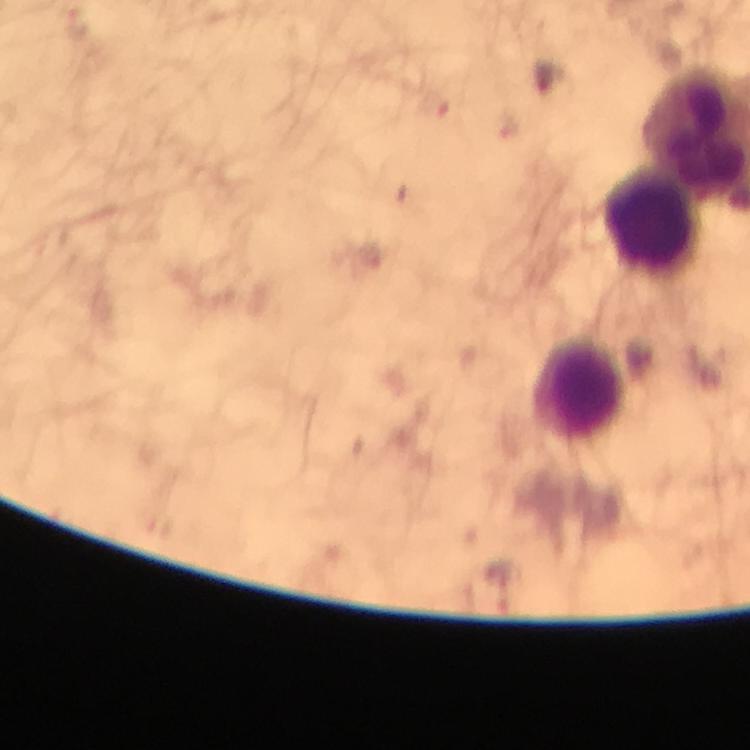

Approximate centers as {x, y} in pixels.
Summary:
  - Leukocyte locations: {653, 221}, {580, 391}
  - Immersion oil: applied
  - Magnification: 100x
  - Preparation: thick smear
  - Capture: smartphone mounted on the microscope
  - Plasmodium parasites: none detected
  - Cropped from: a single field of view
  - Image size: 750×750 pixels
  - Context: from a diagnostic examination for malaria
  - Stain: Giemsa